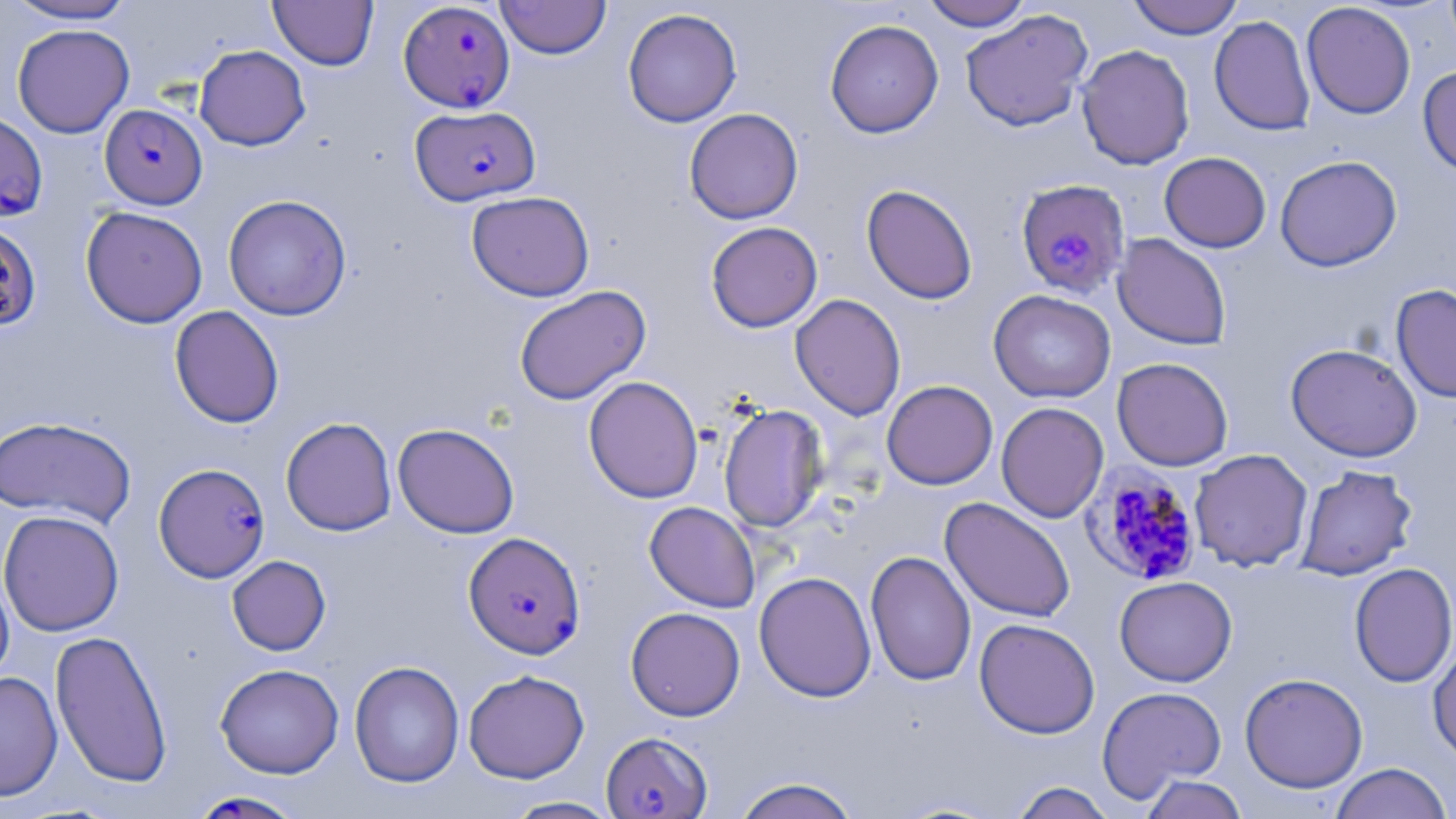

Approximate bounding boxes as (x1, y1, x2, y2) in pixels. Plasmodium falciparum-infected red blood cell locations: (398, 1, 515, 113), (100, 104, 208, 209), (411, 105, 540, 206), (0, 110, 46, 219), (1015, 179, 1130, 299), (0, 221, 42, 332), (154, 463, 270, 582), (1081, 463, 1204, 588), (463, 532, 585, 659), (601, 732, 712, 818), (186, 790, 309, 819). Uninfected red blood cell locations: (3, 0, 139, 25), (269, 0, 379, 70), (495, 0, 611, 59), (921, 0, 1033, 31), (1127, 0, 1243, 39), (1301, 2, 1416, 119), (622, 8, 742, 127), (960, 8, 1094, 132), (1209, 15, 1316, 136), (824, 19, 944, 138), (12, 24, 135, 138), (193, 44, 310, 150), (1076, 44, 1195, 170), (1417, 65, 1456, 178), (684, 108, 803, 224), (1159, 152, 1271, 252), (1275, 155, 1402, 271), (861, 183, 978, 304), (466, 190, 595, 301), (223, 194, 351, 320), (80, 206, 208, 328), (705, 221, 822, 332), (1112, 233, 1232, 350), (1391, 283, 1456, 403), (514, 285, 651, 406), (988, 289, 1116, 403), (789, 293, 906, 420), (169, 305, 284, 428), (1286, 343, 1423, 462), (1112, 357, 1233, 471), (583, 375, 704, 503), (882, 380, 998, 490), (995, 402, 1109, 523), (718, 403, 829, 532), (0, 416, 137, 528), (281, 417, 397, 536), (392, 423, 520, 538), (1189, 449, 1313, 572), (1295, 464, 1418, 581), (940, 497, 1076, 623), (644, 501, 760, 612), (0, 509, 124, 636), (865, 550, 976, 686), (227, 555, 331, 655), (1349, 562, 1456, 688), (0, 568, 15, 687), (754, 571, 876, 702), (1114, 575, 1237, 687), (625, 606, 746, 721), (973, 617, 1100, 739), (50, 629, 173, 789), (1428, 641, 1456, 765), (349, 661, 464, 788), (215, 663, 344, 778), (463, 669, 589, 783), (0, 671, 63, 801), (1239, 672, 1368, 793), (1096, 685, 1226, 802), (1329, 762, 1453, 819), (1139, 774, 1250, 819), (732, 776, 861, 819), (1010, 781, 1116, 819), (501, 796, 622, 818). Slide-level diagnosis: Plasmodium falciparum. Thin blood film. Image is 1456×819 pixels. Captured at 1000x magnification. Single field of view. Optical microscopy. May-Grünwald-Giemsa-stained preparation.